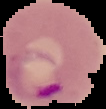
malaria status = parasitized
image type = segmented cell region on a black background
image size = 106×109 pixels
preparation = thin blood smear